State which cell type is depicted.
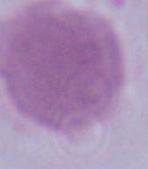
An erythrocyte.

Summary:
  - Modality: photomicrograph
  - Magnification: 1000x